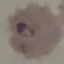

Summary:
  - Result: malaria parasites detected
  - Stain: Giemsa
  - Preparation: thin blood film
  - Image type: cell patch, automatically extracted from a larger field of view and resized to 64 × 64 pixels
  - Capture: smartphone through the microscope eyepiece